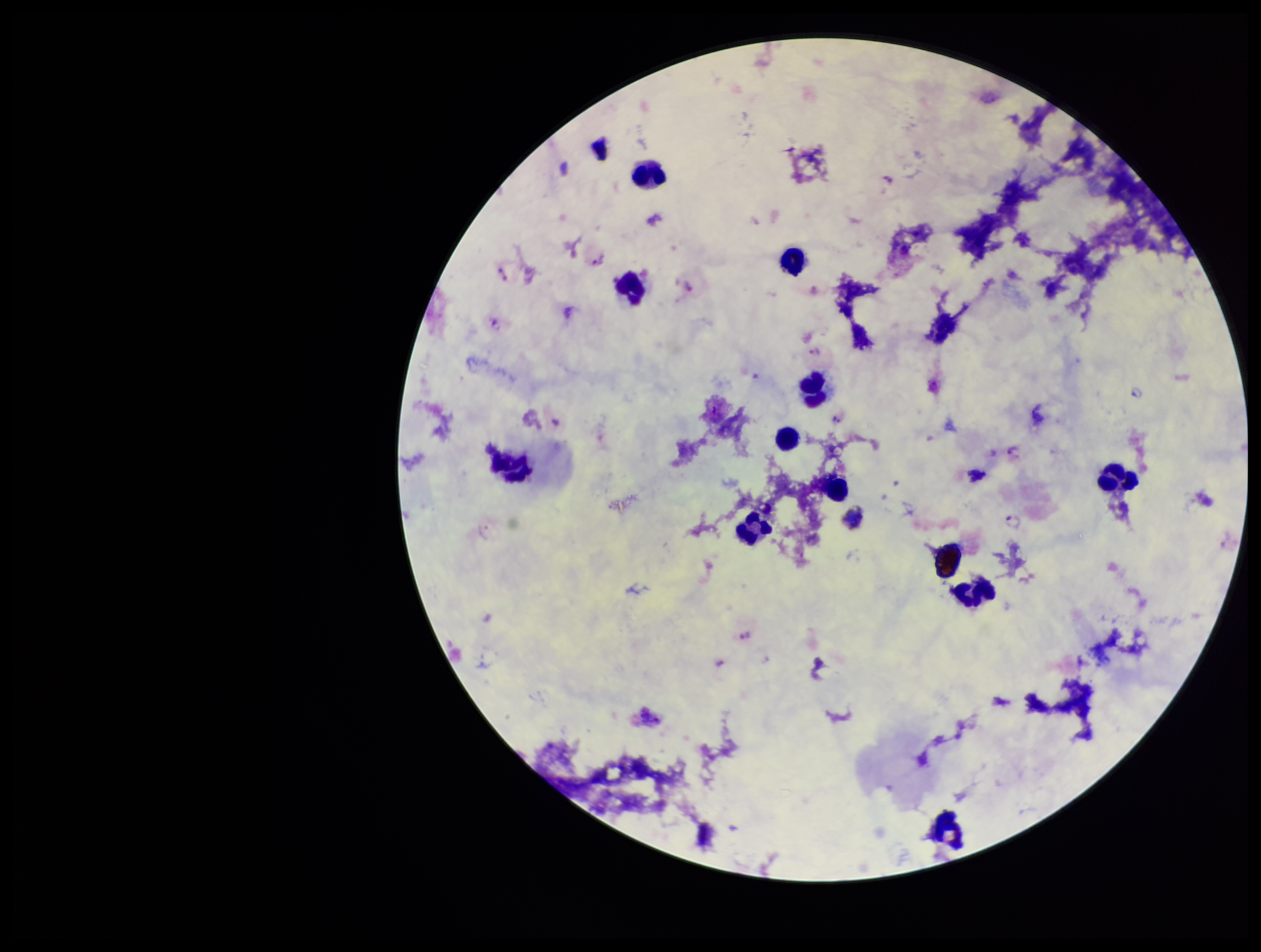

Summary:
  - Species reported for this patient: Plasmodium vivax
  - Stain: Giemsa
  - Parasite count: 9
  - Leukocyte count: 11
  - Preparation: thick
  - Field of view: one from this slide
  - Plasmodium parasites: detected
  - Capture: smartphone photograph through the microscope eyepiece
  - Patient malaria status: infected
  - Image size: 1261×952 pixels